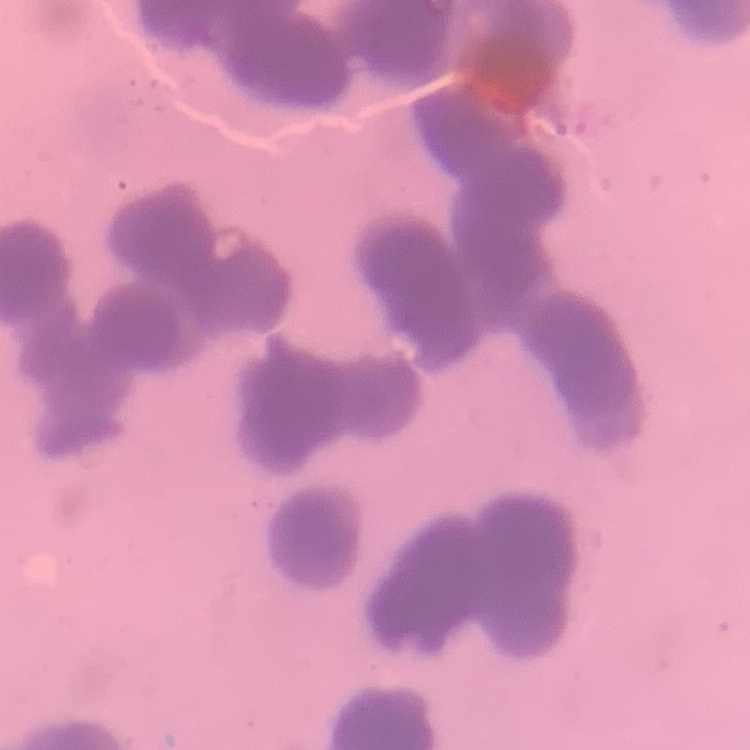
Summary:
  - Erythrocyte morphology: rouleaux formation
  - Image type: one tile cut from a larger photomicrograph
  - Stain: Field's or Giemsa
  - Preparation: thin blood smear